State the blood parasite species.
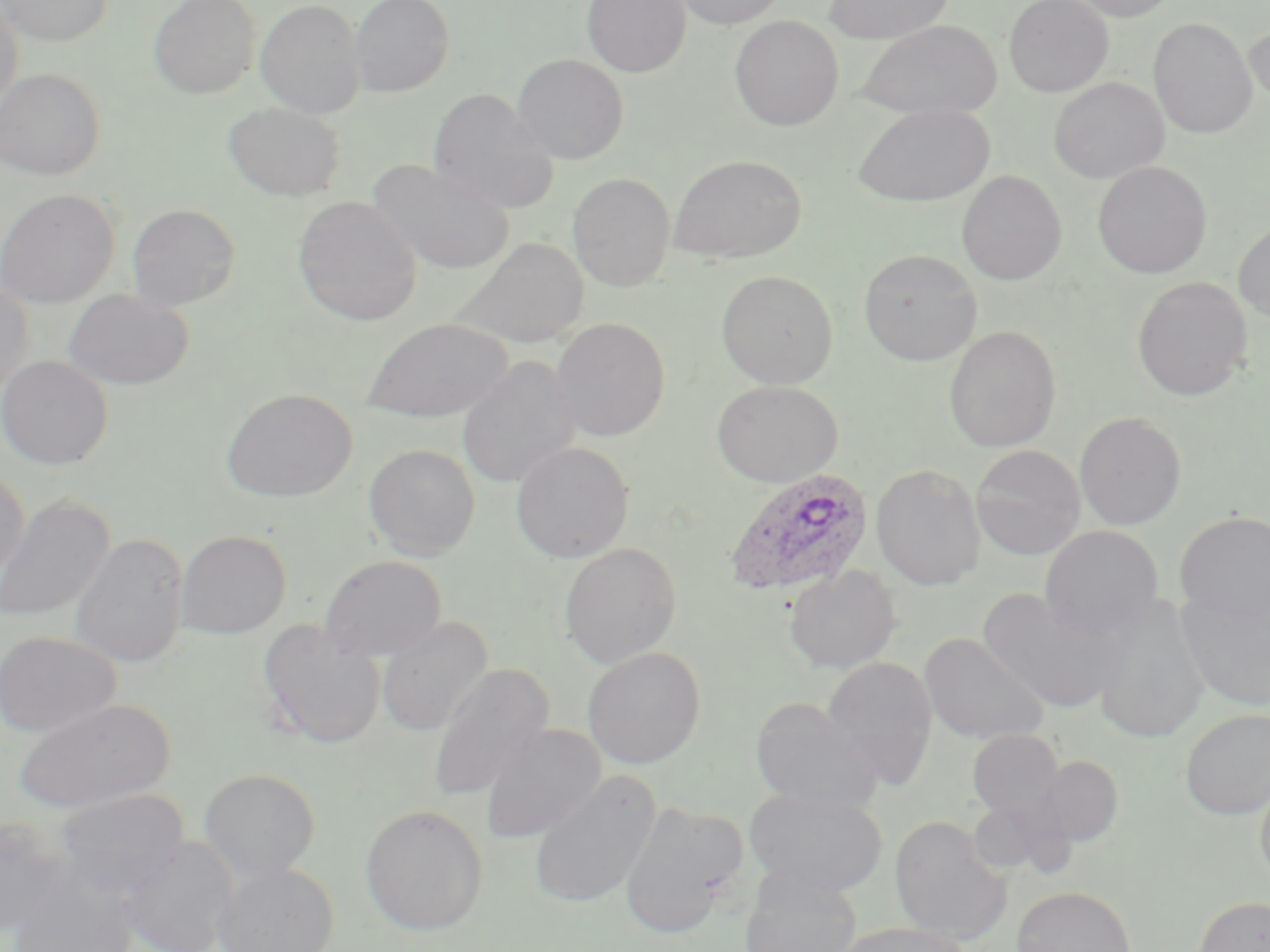
Plasmodium ovale.

field_of_view: one of a larger specimen
plasmodium_ovale_infected_red_blood_cell_locations: 'approximate bounding boxes as named x1/y1/x2/y2 corners in pixels: (x1=724, y1=468, x2=874, y2=599)'
modality: light microscopy
stain: May-Grünwald-Giemsa
image_size: 1270×952 pixels
magnification: 1000x
preparation: thin blood film
uninfected_red_blood_cell_locations: 'approximate bounding boxes as named x1/y1/x2/y2 corners in pixels: (x1=1, y1=0, x2=114, y2=45), (x1=149, y1=0, x2=261, y2=98), (x1=255, y1=0, x2=366, y2=119), (x1=349, y1=0, x2=454, y2=97), (x1=582, y1=0, x2=691, y2=77), (x1=671, y1=0, x2=789, y2=29), (x1=823, y1=0, x2=955, y2=44), (x1=1003, y1=0, x2=1113, y2=97), (x1=1068, y1=0, x2=1179, y2=22), (x1=0, y1=1, x2=24, y2=111), (x1=729, y1=15, x2=844, y2=130), (x1=1148, y1=17, x2=1256, y2=139), (x1=857, y1=20, x2=1002, y2=121), (x1=1244, y1=25, x2=1270, y2=107), (x1=512, y1=54, x2=629, y2=164), (x1=0, y1=67, x2=105, y2=180), (x1=1049, y1=77, x2=1169, y2=183), (x1=427, y1=88, x2=559, y2=215), (x1=223, y1=101, x2=345, y2=201), (x1=852, y1=103, x2=996, y2=207), (x1=668, y1=154, x2=807, y2=264), (x1=367, y1=159, x2=515, y2=275), (x1=1092, y1=160, x2=1213, y2=278), (x1=956, y1=170, x2=1067, y2=285), (x1=567, y1=172, x2=676, y2=291), (x1=0, y1=189, x2=119, y2=309), (x1=293, y1=195, x2=422, y2=327), (x1=126, y1=202, x2=242, y2=311), (x1=1233, y1=219, x2=1270, y2=322), (x1=451, y1=237, x2=589, y2=350), (x1=858, y1=249, x2=982, y2=366), (x1=716, y1=269, x2=839, y2=388), (x1=1131, y1=276, x2=1253, y2=402), (x1=0, y1=278, x2=34, y2=397), (x1=63, y1=288, x2=195, y2=391), (x1=362, y1=317, x2=513, y2=423), (x1=551, y1=317, x2=671, y2=441), (x1=943, y1=324, x2=1062, y2=453), (x1=456, y1=355, x2=582, y2=489), (x1=0, y1=356, x2=113, y2=469), (x1=711, y1=380, x2=843, y2=487), (x1=221, y1=388, x2=357, y2=502), (x1=1074, y1=411, x2=1188, y2=531), (x1=510, y1=441, x2=635, y2=563), (x1=363, y1=443, x2=480, y2=560), (x1=970, y1=444, x2=1086, y2=561), (x1=871, y1=463, x2=986, y2=591), (x1=0, y1=466, x2=30, y2=587), (x1=0, y1=495, x2=115, y2=625), (x1=1175, y1=511, x2=1270, y2=624), (x1=1039, y1=525, x2=1164, y2=640), (x1=175, y1=529, x2=292, y2=639), (x1=69, y1=533, x2=189, y2=669), (x1=559, y1=541, x2=682, y2=669), (x1=319, y1=554, x2=448, y2=662), (x1=785, y1=566, x2=902, y2=675), (x1=978, y1=590, x2=1121, y2=713), (x1=1177, y1=591, x2=1270, y2=711), (x1=1088, y1=595, x2=1210, y2=745), (x1=376, y1=616, x2=493, y2=737), (x1=258, y1=620, x2=386, y2=749), (x1=0, y1=631, x2=121, y2=739), (x1=919, y1=632, x2=1049, y2=745), (x1=582, y1=647, x2=706, y2=770), (x1=821, y1=655, x2=939, y2=785), (x1=426, y1=663, x2=554, y2=805), (x1=749, y1=696, x2=884, y2=813), (x1=13, y1=698, x2=174, y2=816), (x1=1180, y1=707, x2=1270, y2=820), (x1=480, y1=723, x2=606, y2=844), (x1=967, y1=730, x2=1064, y2=822), (x1=1040, y1=755, x2=1124, y2=847), (x1=199, y1=769, x2=320, y2=881), (x1=528, y1=771, x2=661, y2=910), (x1=1255, y1=774, x2=1270, y2=891), (x1=745, y1=786, x2=888, y2=898), (x1=54, y1=788, x2=190, y2=901), (x1=966, y1=796, x2=1065, y2=880), (x1=618, y1=801, x2=746, y2=938), (x1=360, y1=804, x2=488, y2=936), (x1=890, y1=815, x2=1013, y2=946), (x1=0, y1=816, x2=70, y2=936), (x1=119, y1=836, x2=240, y2=952), (x1=212, y1=861, x2=340, y2=952), (x1=738, y1=867, x2=863, y2=952), (x1=8, y1=875, x2=138, y2=952), (x1=1012, y1=886, x2=1137, y2=952), (x1=1191, y1=894, x2=1270, y2=952), (x1=833, y1=922, x2=975, y2=952)'